Outline each blood parasite and name the species.
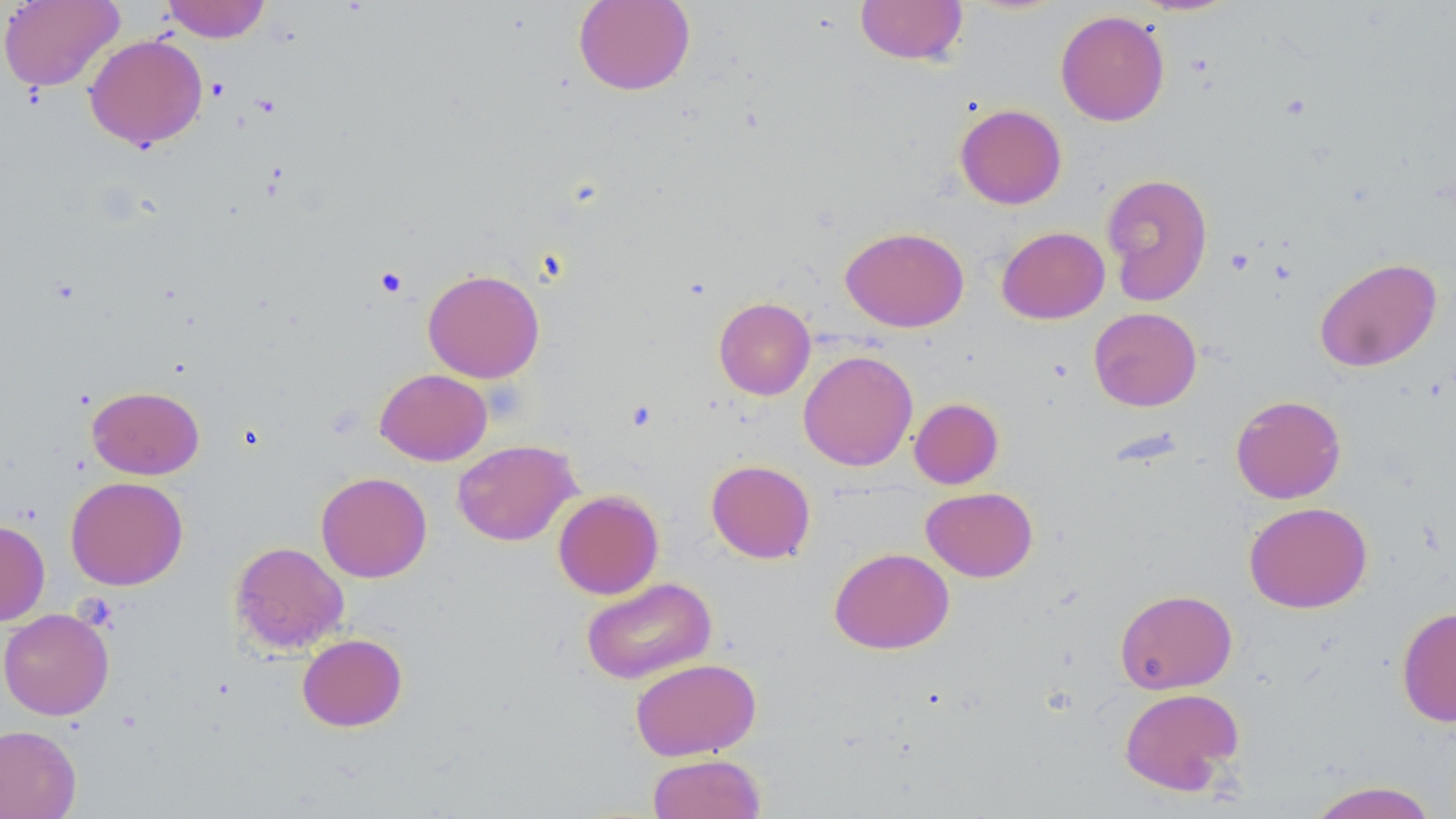

No blood parasites observed.

Approximate bounding boxes as (x1,y1)-(x2,y2) corner pairs in pixels. Platelet locations: (1227,248)-(1255,275), (375,267)-(407,297). Uninfected red blood cell locations: (0,0)-(124,92), (160,0)-(271,42), (573,0)-(695,95), (855,0)-(968,66), (1055,9)-(1170,126), (83,34)-(208,150), (954,103)-(1067,209), (1100,173)-(1213,306), (840,226)-(969,332), (996,226)-(1109,324), (1314,257)-(1442,372), (423,268)-(545,383), (714,297)-(815,400), (1088,307)-(1202,412), (798,350)-(918,471), (375,368)-(492,465), (87,385)-(204,479), (1230,394)-(1346,504), (909,397)-(1004,489), (451,439)-(580,546), (706,460)-(816,563), (315,471)-(432,583), (65,476)-(188,590), (921,486)-(1037,581), (552,490)-(664,599), (1244,501)-(1372,613), (0,519)-(50,625), (230,541)-(349,655), (829,547)-(954,654), (580,577)-(717,684), (1115,588)-(1237,694), (1396,606)-(1456,727), (0,607)-(114,721), (297,633)-(407,732), (630,657)-(761,761), (1119,687)-(1245,796), (0,724)-(82,819), (648,753)-(766,818), (1305,780)-(1440,819). Slide-level diagnosis: negative for blood parasites. One field of a larger specimen. Thin blood smear. May-Grünwald-Giemsa stain. Image is 1456×819 pixels. Light microscopy. 1000x magnification.